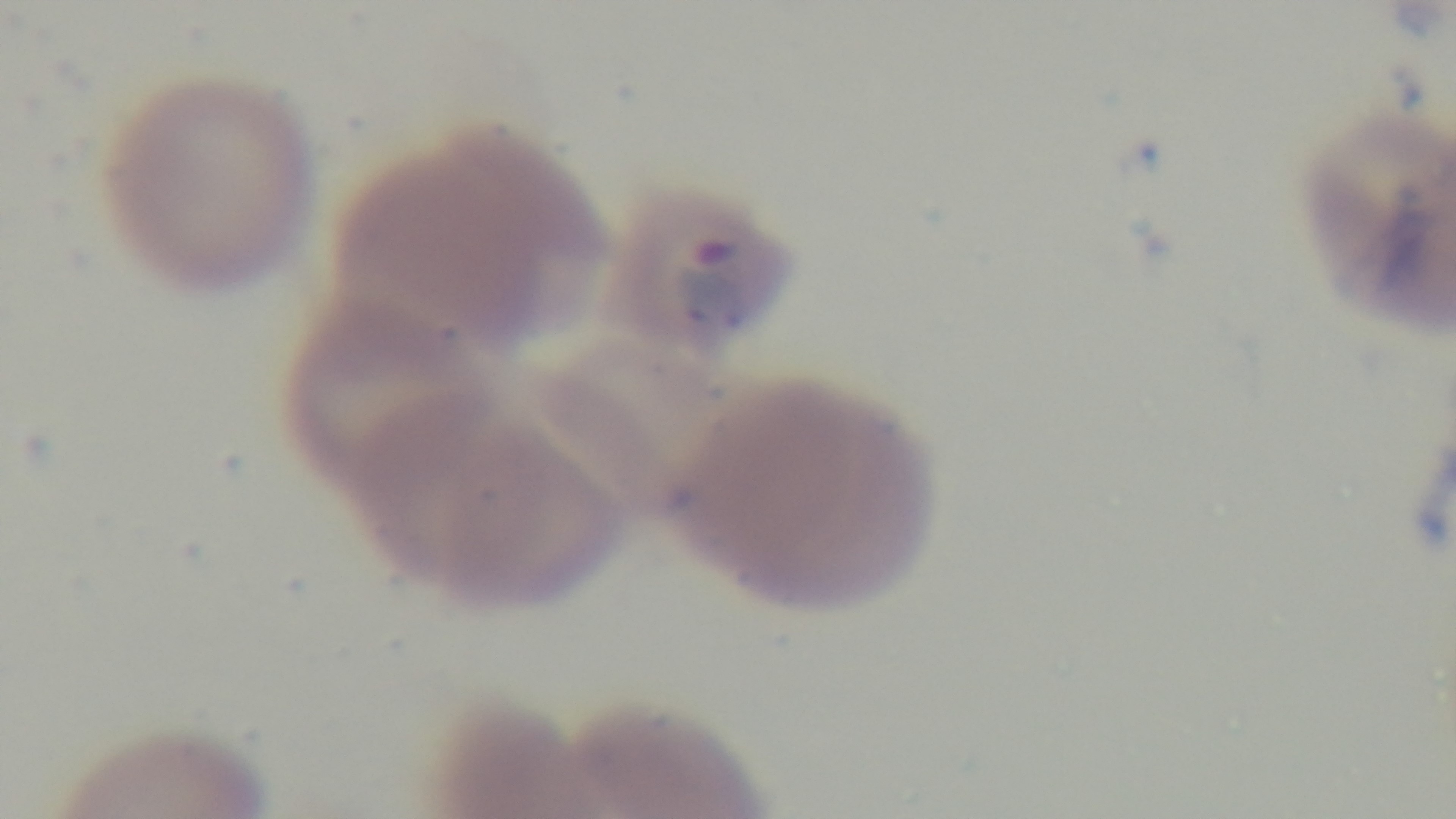
Summary:
  - Malaria status: positive
  - Capture: mounted 4K digital camera
  - Stain: Giemsa
  - Objective: 100x oil immersion
  - Field of view: one from the slide
  - Preparation: thin smear
  - Modality: light microscopy